Locate every leukocyte (white blood cell).
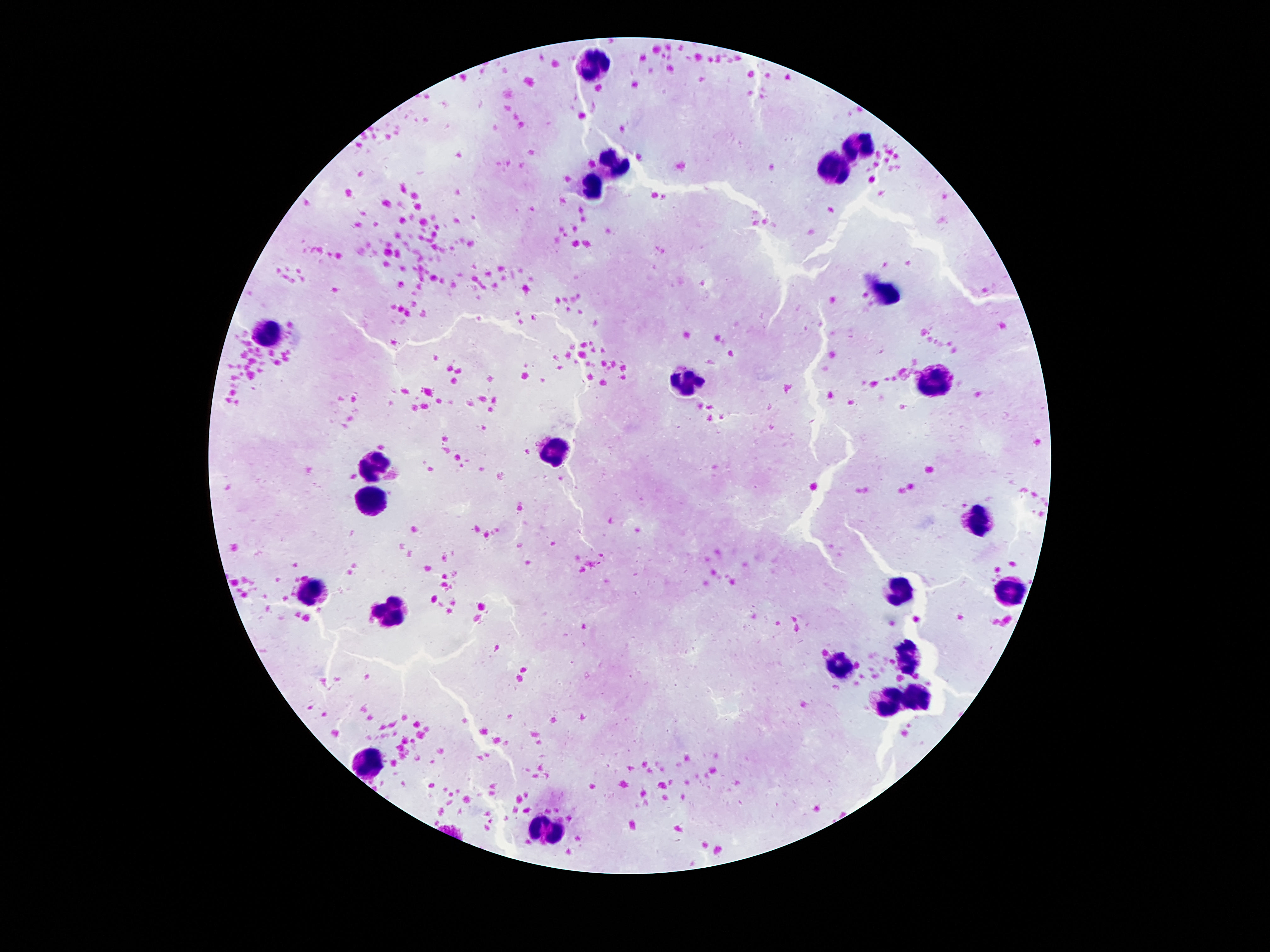
Approximate centers as {x, y} in pixels.
Leukocytes: {589, 63}, {862, 147}, {614, 161}, {836, 169}, {593, 185}, {888, 295}, {272, 331}, {939, 379}, {690, 381}, {556, 448}, {382, 463}, {369, 504}, {980, 519}, {1010, 588}, {313, 590}, {897, 590}, {390, 608}, {909, 656}, {841, 662}, {918, 698}, {890, 703}, {371, 763}, {545, 830}.

{
  "magnification": "100x",
  "capture": "smartphone camera through the microscope eyepiece",
  "stain": "Giemsa",
  "field_of_view": "single",
  "preparation": "thick blood film",
  "image_size": "1270×952 pixels",
  "patient_malaria_status": "uninfected"
}